Classify the preparation.
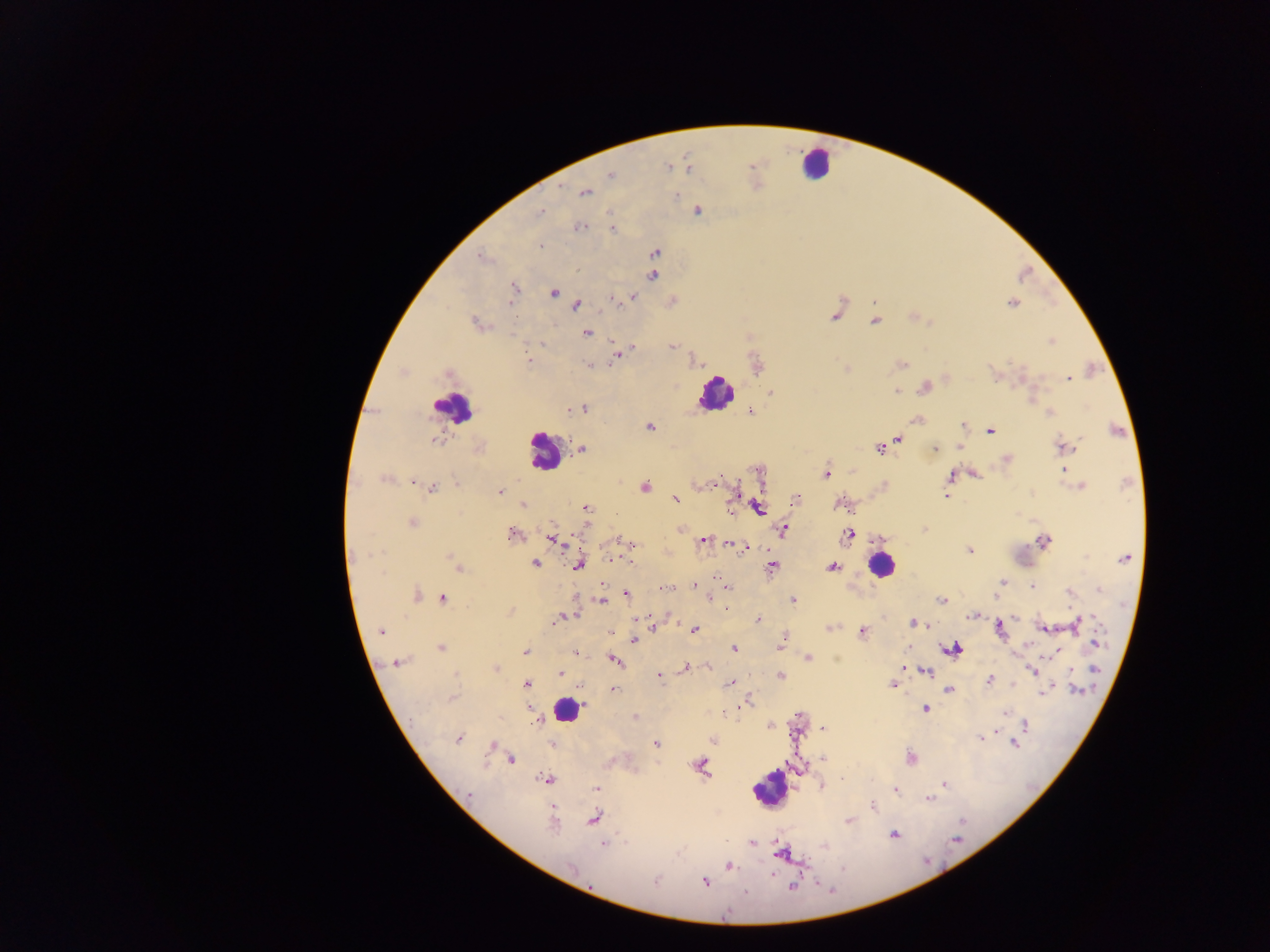
Thick blood smear.

Approximate centers as x y in pixels.
Summary:
  - Malaria parasite locations: 687 166; 668 167; 610 175; 585 192; 697 210; 539 212; 577 228; 613 228; 540 246; 654 252; 481 256; 654 264; 652 275; 513 287; 552 292; 632 296; 612 298; 671 301; 1012 303; 576 305; 836 314; 914 317; 875 320; 476 323; 586 332; 1052 340; 672 345; 617 352; 528 359; 694 360; 590 364; 901 364; 757 366; 844 368; 449 373; 946 377; 1068 377; 924 386; 895 391; 770 393; 571 408; 581 408; 750 410; 1049 412; 917 419; 648 426; 963 426; 989 430; 434 439; 897 439; 479 447; 881 447; 960 447; 1063 447; 934 448; 581 449; 1006 459; 758 470; 1062 470; 826 473; 972 474; 951 477; 385 478; 414 481; 457 484; 1081 486; 643 487; 431 488; 500 491; 733 494; 947 495; 676 498; 795 498; 523 504; 840 504; 757 507; 586 508; 412 522; 680 527; 925 528; 782 529; 511 533; 848 535; 552 538; 702 539; 1044 541; 631 543; 730 544; 739 546; 746 547; 969 550; 609 559; 1124 559; 630 562; 534 563; 457 565; 577 565; 771 566; 832 566; 1002 582; 693 584; 1033 585; 665 588; 727 589; 1099 589; 1069 591; 624 593; 415 595; 442 598; 709 598; 792 599; 601 600; 940 600; 727 605; 510 610; 972 613; 563 616; 758 620; 1075 623; 914 624; 652 627; 1000 627; 828 628; 1043 628; 693 630; 381 631; 611 631; 861 631; 634 639; 781 642; 1094 643; 440 648; 734 648; 952 649; 525 651; 1056 652; 575 653; 808 657; 614 660; 397 662; 708 666; 495 668; 685 668; 900 669; 1032 670; 1071 671; 926 672; 559 673; 659 675; 780 676; 988 680; 730 683; 527 684; 1013 684; 892 685; 581 686; 613 688; 949 688; 1048 688; 1044 692; 451 697; 745 701; 925 708; 1002 712; 635 717; 1025 725; 770 726; 822 728; 458 737; 712 739; 980 739; 552 742; 1014 742; 656 744; 492 745; 909 757; 822 758; 509 759; 700 766; 546 778; 823 783; 944 784; 596 788; 893 789; 929 799; 872 806; 594 818; 553 819; 848 821; 894 834; 752 842; 603 844; 781 853; 728 866; 772 874; 705 881
  - Leukocyte locations: 815 164; 717 392; 453 406; 544 451; 882 564; 567 710; 769 788
  - Capture: mobile-phone photograph through a microscope
  - Country: Ghana
  - Image size: 1270×952 pixels
  - Field of view: single